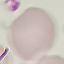

Malaria status: uninfected. Thin blood film. Automatically extracted cell patch, resized to 64 × 64 pixels. Photographed with a smartphone camera at the microscope eyepiece. Giemsa stain.